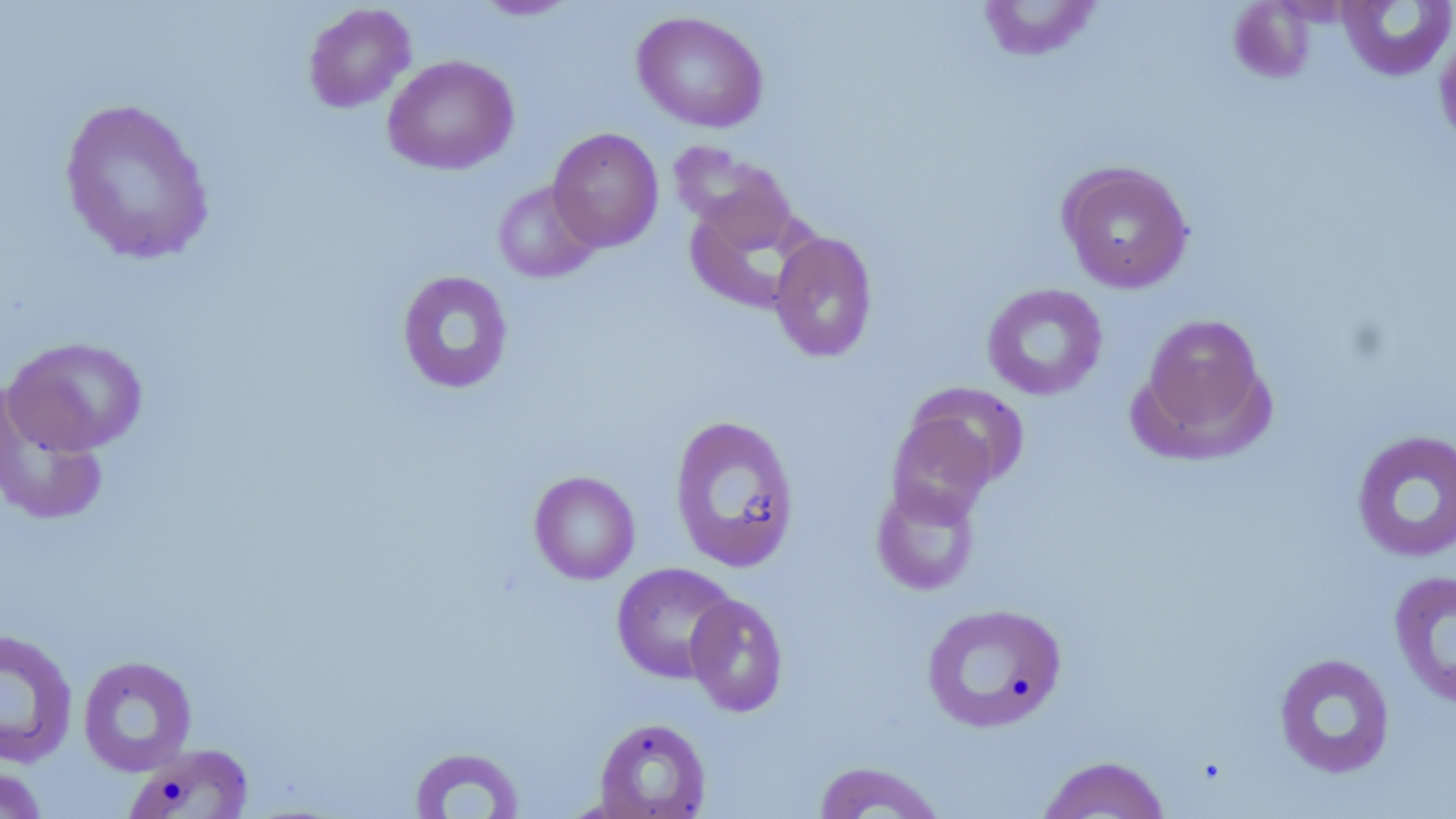
slide-level diagnosis = no evidence of blood parasites
preparation = thin blood smear
stain = May-Grünwald-Giemsa
magnification = 1000x
modality = light microscopy
uninfected red blood cell locations = approximate bounding boxes as (x1,y1)-(x2,y2) corner pairs in pixels: (473,0)-(582,20), (976,0)-(1103,62), (1228,1)-(1316,83), (1336,1)-(1456,81), (302,3)-(416,113), (631,11)-(769,133), (1434,29)-(1456,149), (382,55)-(519,175), (58,97)-(216,266), (547,127)-(664,251), (673,145)-(799,257), (1057,161)-(1195,293), (492,180)-(601,283), (769,231)-(878,363), (397,270)-(513,394), (981,282)-(1108,400), (1135,312)-(1273,457), (3,336)-(149,455), (0,383)-(110,527), (907,383)-(1030,490), (886,412)-(998,524), (668,414)-(800,573), (1351,429)-(1456,563), (529,470)-(641,585), (871,481)-(981,596), (611,562)-(738,683), (1388,570)-(1456,709), (684,593)-(788,717), (921,602)-(1067,734), (0,627)-(79,769), (1273,652)-(1396,779), (77,655)-(198,776), (593,716)-(712,818), (124,742)-(254,818), (408,746)-(526,818), (1037,755)-(1172,818), (812,760)-(947,818), (0,764)-(49,819)
field of view = single
image size = 1456×819 pixels